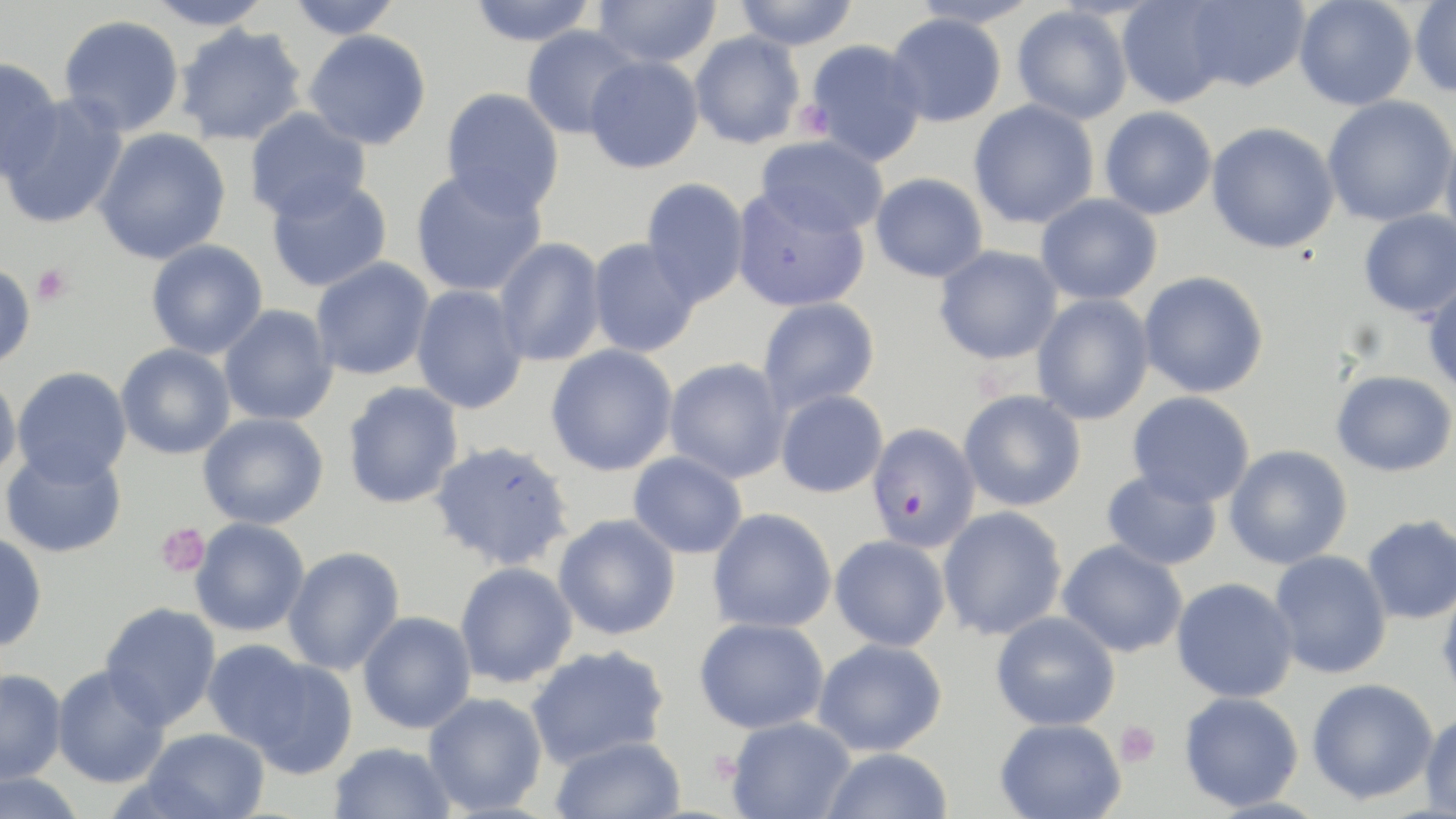

slide-level diagnosis = Plasmodium falciparum
magnification = 1000x
platelet locations = approximate bounding boxes as [x1, y1, x2, y2] in pixels: [795, 99, 835, 141], [31, 263, 73, 306], [155, 522, 210, 578], [1114, 720, 1160, 767]
field of view = one of a larger specimen
preparation = thin blood film
modality = optical microscopy
image size = 1456×819 pixels
uninfected red blood cell locations = approximate bounding boxes as [x1, y1, x2, y2] in pixels: [144, 0, 276, 31], [285, 0, 404, 40], [466, 0, 598, 46], [593, 0, 722, 68], [732, 0, 860, 50], [1294, 0, 1418, 111], [908, 1, 1041, 28], [1116, 1, 1234, 108], [1180, 1, 1309, 92], [1409, 1, 1456, 98], [1012, 6, 1133, 125], [885, 12, 1007, 127], [58, 14, 184, 137], [173, 23, 308, 146], [521, 24, 641, 139], [303, 29, 432, 150], [689, 31, 806, 149], [805, 39, 927, 167], [585, 56, 704, 173], [0, 58, 63, 180], [440, 87, 565, 216], [0, 93, 129, 230], [1322, 94, 1456, 227], [968, 100, 1099, 229], [1099, 106, 1217, 220], [244, 107, 371, 222], [1206, 121, 1340, 254], [1440, 126, 1456, 249], [92, 128, 231, 265], [756, 135, 889, 237], [409, 167, 547, 298], [870, 172, 988, 282], [265, 175, 392, 293], [640, 177, 750, 307], [731, 185, 870, 313], [1035, 193, 1162, 305], [1358, 209, 1456, 319], [587, 237, 700, 358], [494, 238, 606, 367], [146, 240, 268, 359], [933, 245, 1062, 364], [310, 257, 434, 380], [0, 263, 35, 369], [1138, 270, 1269, 398], [1422, 277, 1456, 397], [411, 284, 528, 414], [1032, 294, 1154, 425], [757, 297, 880, 414], [218, 304, 338, 426], [115, 343, 236, 459], [545, 344, 678, 476], [663, 358, 791, 484], [12, 367, 132, 486], [1331, 370, 1456, 477], [0, 371, 22, 484], [342, 382, 464, 509], [776, 389, 888, 498], [958, 389, 1087, 512], [1126, 391, 1256, 508], [198, 413, 328, 529], [429, 439, 574, 571], [1224, 444, 1352, 570], [1, 447, 127, 557], [628, 451, 748, 559], [1101, 468, 1223, 571], [937, 506, 1067, 640], [707, 507, 837, 634], [553, 514, 680, 640], [1362, 515, 1456, 624], [190, 518, 310, 637], [0, 532, 48, 652], [830, 534, 950, 651], [1057, 540, 1188, 658], [282, 546, 405, 676], [1269, 550, 1392, 679], [454, 561, 578, 688], [1171, 577, 1299, 703], [1436, 584, 1456, 710], [100, 602, 221, 730], [358, 611, 476, 734], [991, 611, 1121, 731], [694, 617, 828, 734], [812, 637, 948, 756], [201, 639, 312, 751], [526, 645, 670, 769], [247, 658, 359, 780], [51, 664, 171, 788], [0, 668, 67, 785], [1306, 678, 1439, 805], [1178, 691, 1304, 811], [423, 692, 548, 815], [1419, 711, 1456, 818], [726, 716, 857, 819], [995, 718, 1126, 818], [141, 727, 270, 819], [550, 735, 687, 819], [329, 742, 456, 819], [819, 747, 953, 819], [0, 771, 88, 819]
Plasmodium falciparum-infected red blood cell locations = approximate bounding boxes as [x1, y1, x2, y2] in pixels: [866, 423, 980, 551]
stain = May-Grünwald-Giemsa